Name the cell type shown.
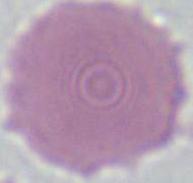

An erythrocyte.

Captured at 1000x magnification. Micrograph.